Assess this cell for malaria.
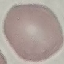

It is uninfected.

{
  "stain": "Giemsa",
  "capture": "smartphone camera at the microscope eyepiece",
  "preparation": "thin blood smear",
  "image_type": "cell patch, automatically extracted from a larger field of view and resized to 64 × 64 pixels"
}